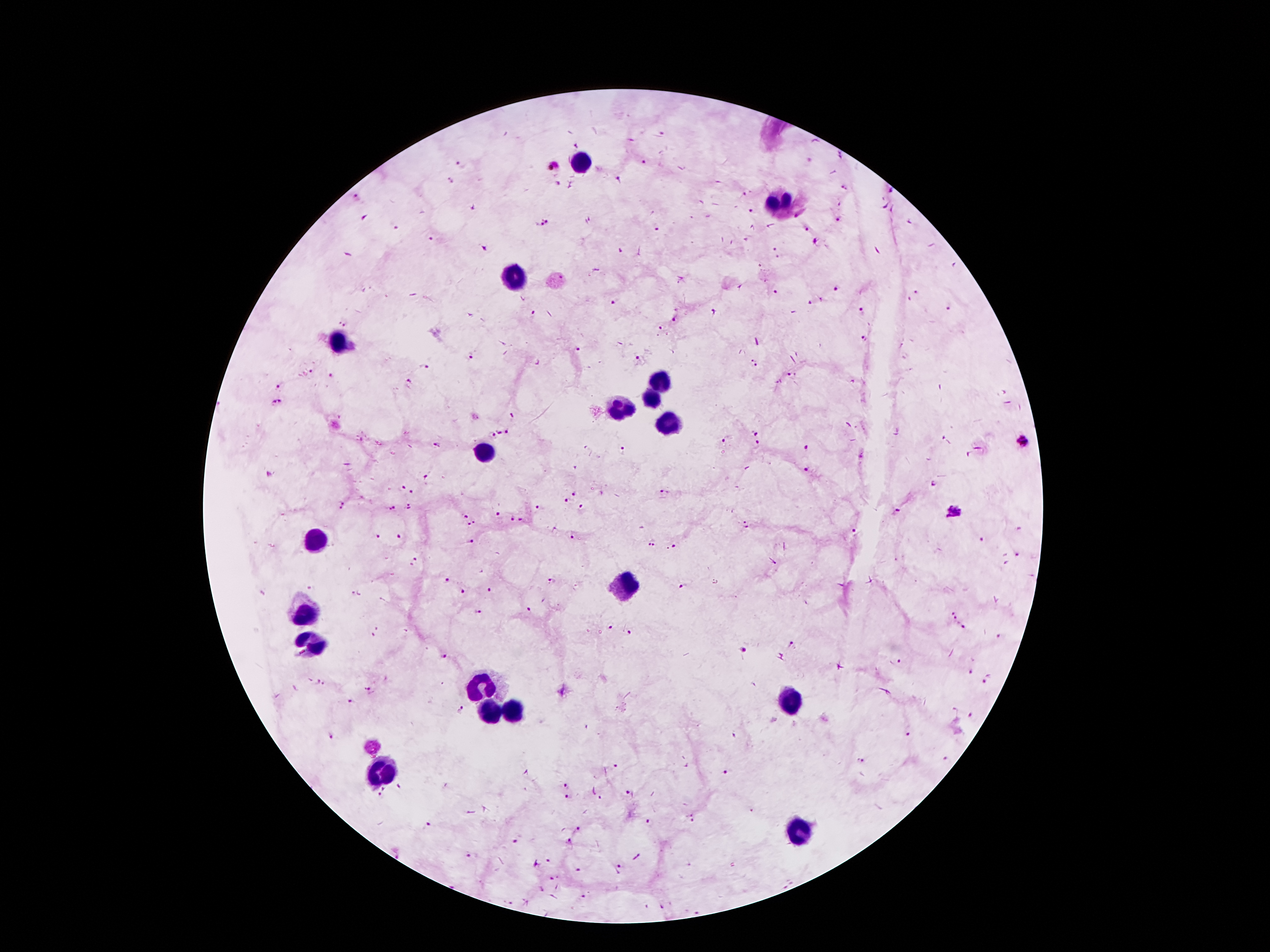

coordinate format = approximate centers as [x, y] in pixels
leukocyte locations = [582, 162], [780, 205], [515, 280], [337, 339], [658, 381], [654, 397], [623, 408], [668, 418], [487, 453], [315, 537], [626, 590], [308, 611], [315, 643], [478, 686], [789, 701], [487, 708], [511, 713], [386, 772], [801, 831]
malaria parasite locations = [663, 132], [462, 162], [643, 164], [554, 165], [617, 179], [844, 190], [890, 192], [356, 198], [751, 210], [838, 220], [546, 221], [395, 227], [658, 228], [806, 228], [433, 238], [814, 240], [774, 249], [836, 288], [776, 292], [917, 292], [909, 298], [614, 300], [811, 302], [949, 309], [862, 312], [536, 314], [674, 320], [344, 322], [661, 327], [866, 339], [579, 349], [469, 356], [638, 358], [752, 364], [427, 366], [311, 371], [332, 375], [792, 375], [409, 383], [275, 387], [276, 402], [512, 416], [497, 433], [492, 434], [508, 434], [757, 434], [726, 440], [1022, 441], [436, 445], [756, 445], [804, 448], [624, 452], [806, 470], [427, 476], [402, 485], [934, 487], [665, 493], [412, 494], [574, 495], [565, 502], [341, 504], [409, 506], [393, 507], [582, 508], [540, 509], [955, 512], [463, 513], [897, 513], [497, 514], [512, 519], [522, 520], [472, 524], [744, 525], [854, 531], [379, 534], [399, 537], [573, 537], [983, 539], [472, 541], [651, 543], [675, 546], [1018, 554], [414, 563], [445, 582], [552, 583], [682, 585], [489, 589], [463, 591], [478, 610], [531, 611], [953, 615], [610, 626], [965, 628], [378, 633], [630, 634], [999, 637], [791, 645], [742, 650], [443, 658], [898, 663], [969, 674], [987, 679], [320, 683], [371, 691], [352, 702], [462, 709], [970, 715], [907, 732], [332, 736], [862, 761], [614, 766], [727, 772], [400, 786], [565, 786], [382, 792], [627, 792], [568, 797], [601, 797], [692, 817], [430, 823], [651, 823], [578, 829], [516, 840], [567, 841], [475, 855], [548, 860], [620, 865], [580, 871], [555, 877], [787, 885], [582, 897], [663, 907], [698, 910]
capture = smartphone camera through the microscope eyepiece
image size = 1270×952 pixels
field of view = single
patient malaria status = positive for Plasmodium falciparum
stain = Giemsa
magnification = 100x
preparation = thick blood smear